Assess this cell for malaria.
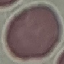
Uninfected.

Summary:
  - Preparation: thin blood smear
  - Image type: automatically extracted cell patch, resized to 64 × 64 pixels
  - Capture: smartphone through the microscope eyepiece
  - Stain: Giemsa